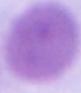
A red blood cell is shown. Micrograph. Captured at 1000x magnification.